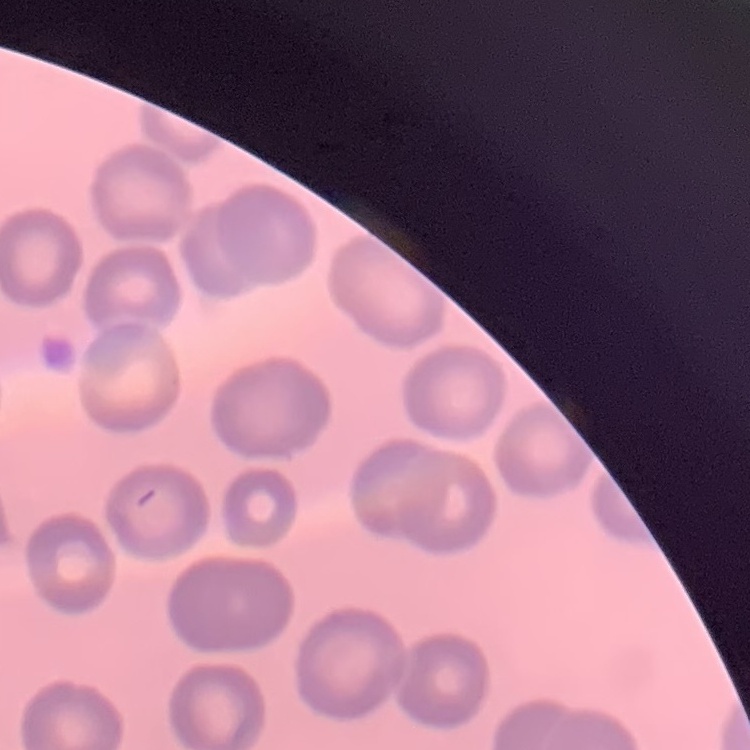

Summary:
  - Erythrocyte morphology: no rouleaux formation
  - Stain: Field's or Giemsa
  - Preparation: thin blood smear
  - Image type: square crop of a larger photomicrograph